Report the malaria status of this cell.
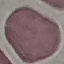

It is uninfected.

Giemsa stain. Acquired by smartphone through the microscope eyepiece. Thin blood smear. Automatically extracted cell patch, resized to 64 × 64 pixels.